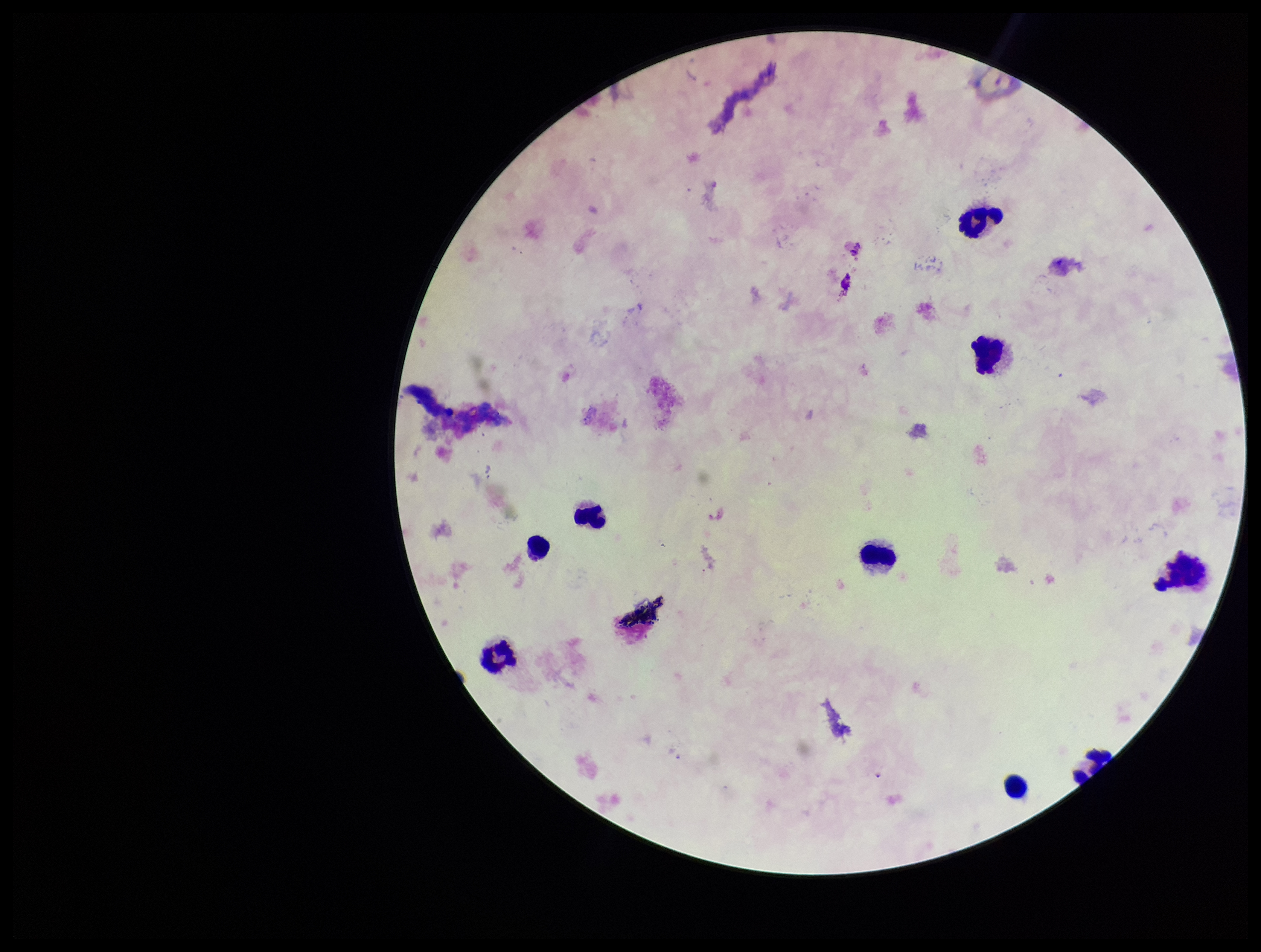
Summary:
  - Capture: smartphone photograph through the microscope eyepiece
  - Species reported for this patient: Plasmodium falciparum
  - Image size: 1261×952 pixels
  - Plasmodium parasites: none seen
  - Leukocyte count: 9
  - Preparation: thick smear
  - Field of view: one from this slide
  - Patient malaria status: infected
  - Stain: Giemsa
  - Parasite count: 0